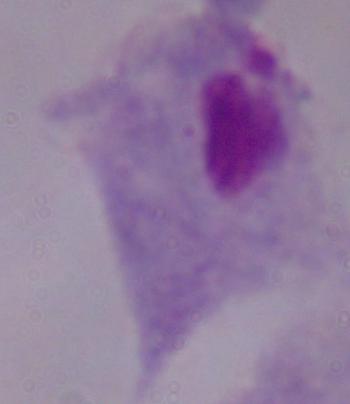
Summary:
  - Identification: trichomonad
  - Modality: photomicrograph
  - Magnification: 1000x